Assess this cell for malaria.
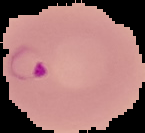
Parasitized.

From a thin blood film. Cell region segmented out of the field of view; the surrounding area is masked to black. Image is 145×133 pixels.